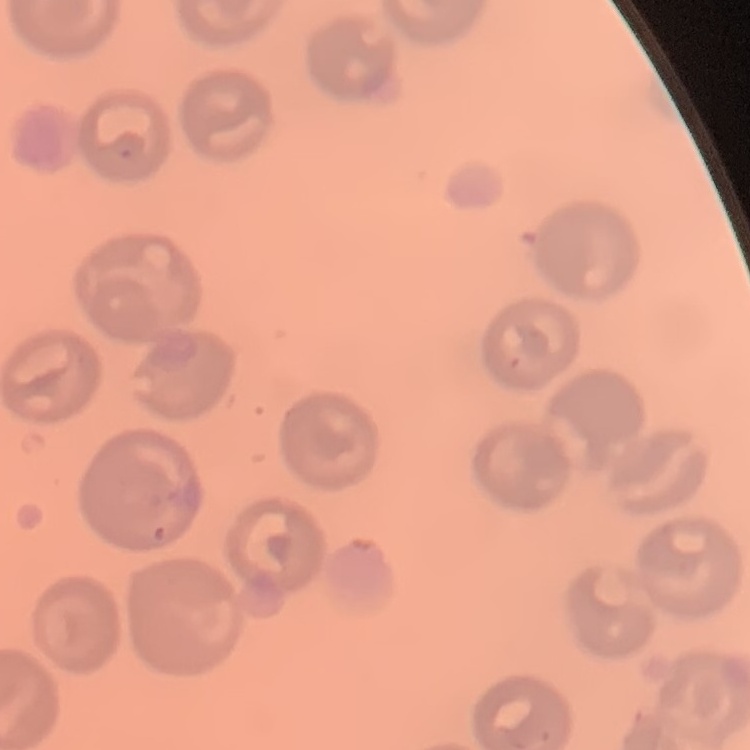

The erythrocytes show no rouleaux formation. Square crop of a larger photomicrograph. Thin blood film. Stained with either Field's or Giemsa.